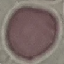

Malaria status: uninfected. Automatically extracted cell patch, resized to 64 × 64 pixels. Thin blood film. Giemsa-stained preparation. Acquired by smartphone through the microscope eyepiece.